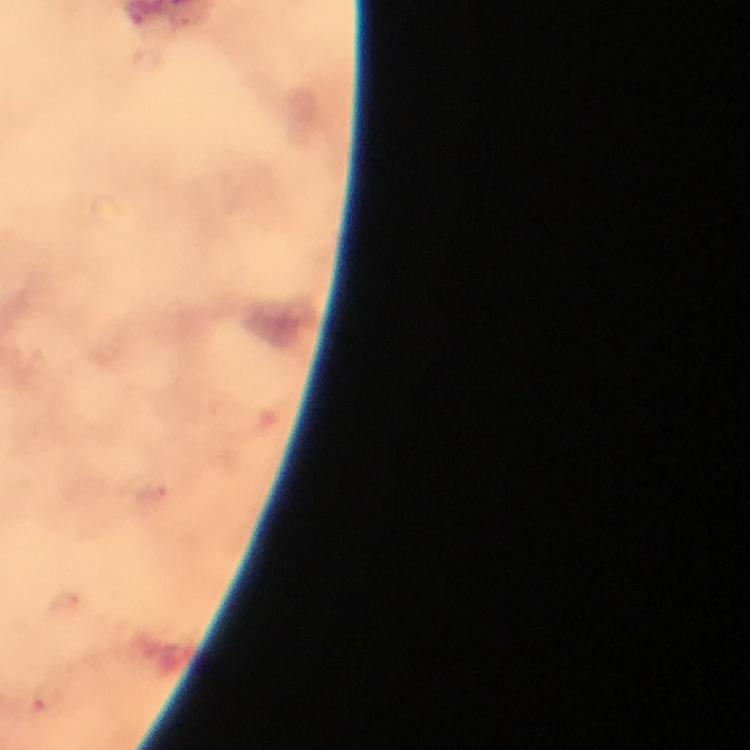

Approximate object centers, in pixels from the top-left corner.
Summary:
  - Plasmodium parasite locations: (x=151, y=494), (x=64, y=602), (x=45, y=700)
  - Image size: 750×750 pixels
  - Stain: Giemsa
  - Preparation: thick blood smear
  - Immersion oil: applied
  - Magnification: 100x
  - Context: from a diagnostic examination for malaria
  - Capture: smartphone photograph through a microscope
  - Cropped from: one field of view